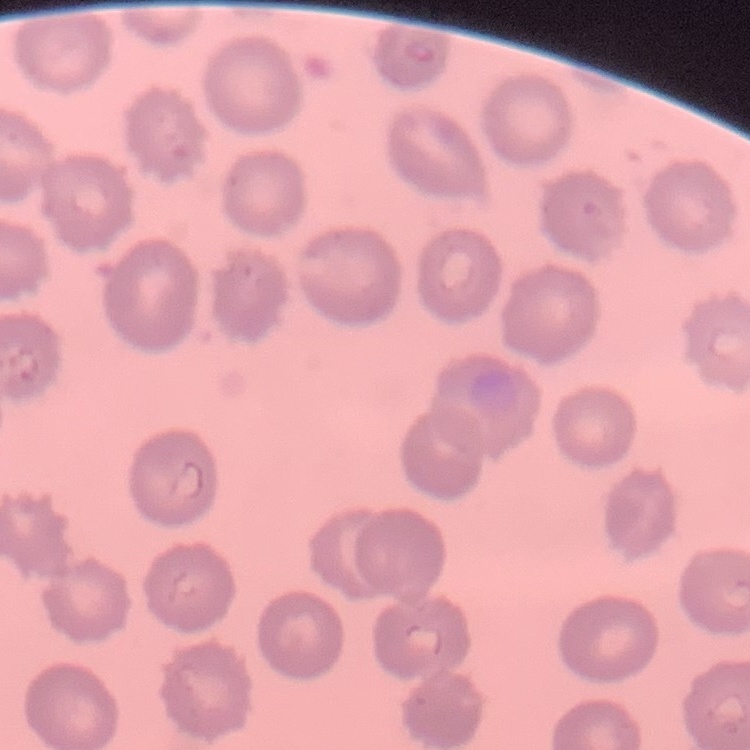

Summary:
  - Erythrocyte morphology: no rouleaux formation
  - Stain: Field's or Giemsa
  - Preparation: thin blood film
  - Image type: square crop of a larger photomicrograph